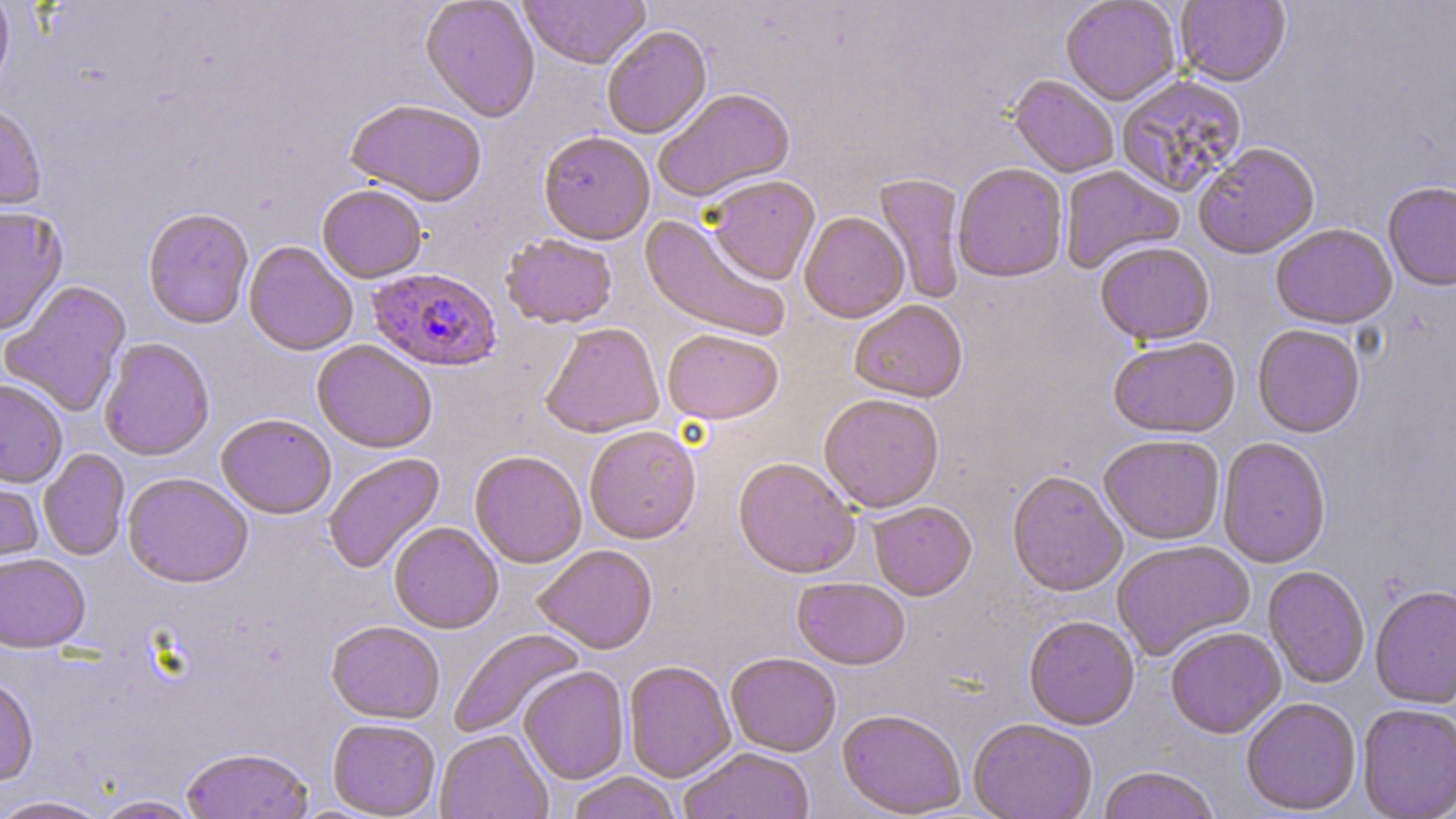

{
  "slide_level_diagnosis": "Plasmodium falciparum",
  "modality": "light microscopy",
  "stain": "May-Grünwald-Giemsa",
  "uninfected_red_blood_cell_locations": "approximate bounding boxes as (x1,y1)-(x2,y2) corner pairs in pixels: (421,0)-(540,122), (518,0)-(650,69), (1061,0)-(1181,105), (1175,0)-(1291,87), (0,1)-(15,98), (602,26)-(712,140), (1009,75)-(1119,178), (1115,77)-(1248,200), (653,88)-(795,203), (345,100)-(487,207), (0,103)-(46,215), (538,131)-(655,245), (1193,143)-(1320,259), (953,163)-(1068,282), (1059,165)-(1184,274), (873,174)-(966,304), (705,176)-(820,286), (1382,181)-(1456,292), (317,184)-(427,283), (0,206)-(68,337), (142,208)-(253,330), (799,213)-(909,323), (640,215)-(790,341), (1270,223)-(1397,329), (143,229)-(357,342), (501,234)-(618,330), (244,241)-(358,356), (1095,241)-(1215,345), (0,280)-(132,418), (849,300)-(968,402), (540,322)-(664,439), (1252,324)-(1365,438), (662,329)-(784,424), (1108,335)-(1241,438), (98,338)-(214,461), (312,340)-(437,453), (0,377)-(68,487), (818,393)-(944,512), (216,414)-(336,518), (584,425)-(701,544), (1098,434)-(1225,545), (1217,437)-(1331,568), (38,449)-(130,561), (469,450)-(587,568), (323,452)-(445,575), (733,458)-(860,579), (0,467)-(44,571), (1007,469)-(1127,597), (123,472)-(253,588), (867,501)-(977,601), (389,522)-(503,633), (1112,540)-(1254,662), (533,544)-(658,654), (0,552)-(90,653), (1263,566)-(1370,689), (792,577)-(911,670), (1369,584)-(1456,709), (1024,615)-(1140,730), (326,620)-(445,723), (1165,627)-(1286,739), (449,629)-(585,740), (726,653)-(841,757), (623,660)-(736,782), (518,666)-(629,785), (0,676)-(39,787), (1241,697)-(1361,815), (1357,703)-(1456,818), (837,709)-(966,818), (327,718)-(441,817), (968,719)-(1098,819), (435,729)-(553,819), (181,746)-(313,819), (678,748)-(814,819), (1097,766)-(1220,819), (567,772)-(681,819), (0,795)-(112,819), (91,795)-(204,818)",
  "magnification": "1000x",
  "preparation": "thin blood smear",
  "field_of_view": "single",
  "image_size": "1456×819 pixels",
  "plasmodium_falciparum_infected_red_blood_cell_locations": "approximate bounding boxes as (x1,y1)-(x2,y2) corner pairs in pixels: (367,267)-(502,372)"
}